Identify the parasite.
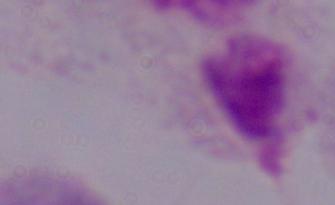
A trichomonad.

Photomicrograph. 1000x magnification.